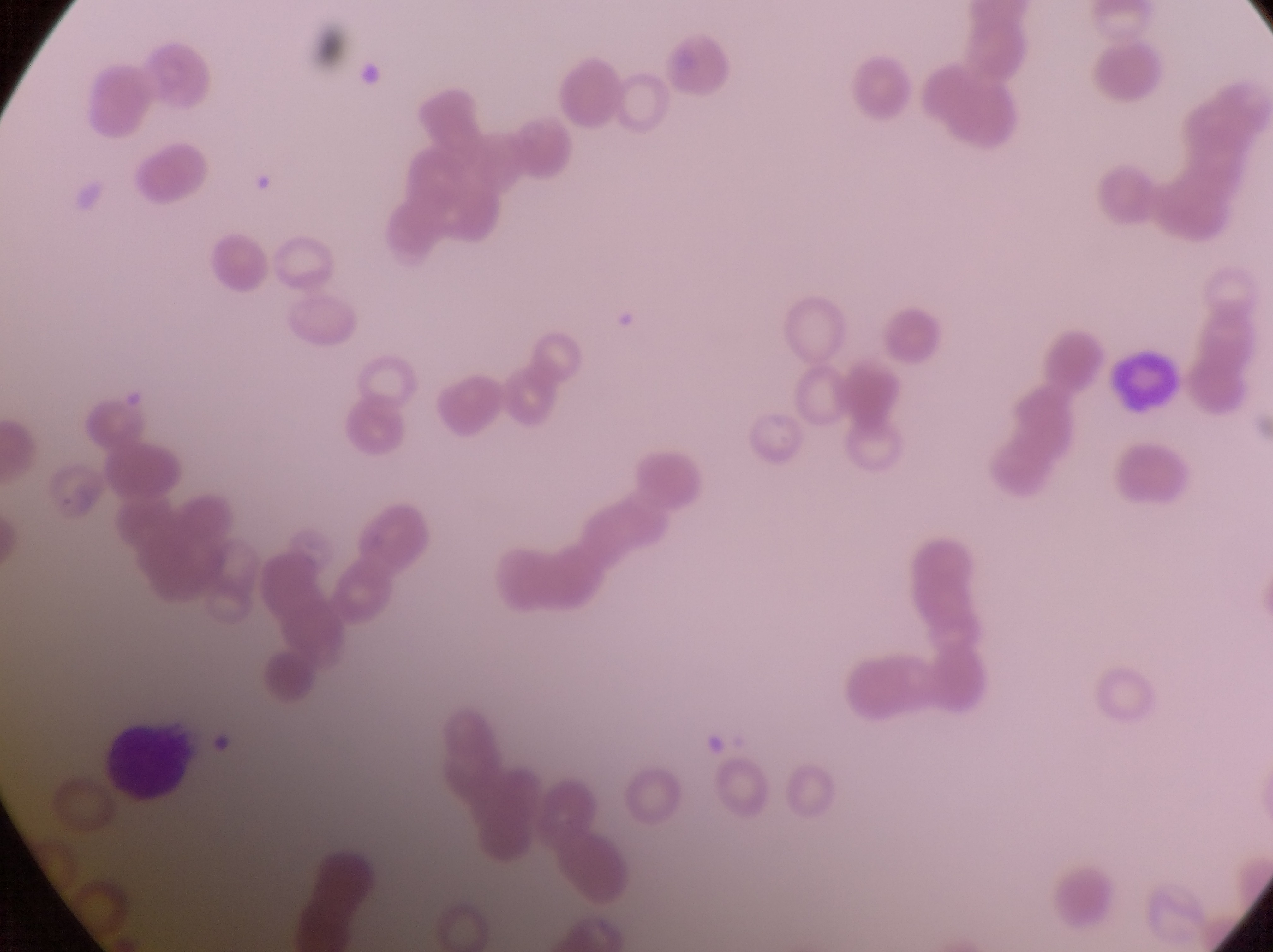

country: Uganda
capture: smartphone photograph through the eyepiece of an Olympus CX-23 microscope
artifact_platelet_like_body_stain_precipitate_or_debris_locations: 'approximate bounding boxes as {left, top, right, bottom} in pixels: {354, 57, 391, 105}, {245, 169, 275, 201}'
leukocyte_locations: 'approximate bounding boxes as {left, top, right, bottom} in pixels: {1109, 347, 1184, 421}, {100, 717, 199, 810}'
image_size: 1273×952 pixels
magnification: 1000x
preparation: thin blood film
field_of_view: single